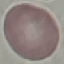
Result: negative for malaria parasites. Acquired by smartphone through the microscope eyepiece. Thin blood smear. Cell patch, automatically extracted from a larger field of view and resized to 64 × 64 pixels. Giemsa stain.